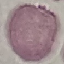
malaria status = uninfected
stain = Giemsa
preparation = thin blood smear
capture = smartphone through the microscope eyepiece
image type = automatically extracted cell patch, resized to 64 × 64 pixels